Identify the cell.
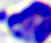

This is a leukocyte.

Photomicrograph. 400x magnification.